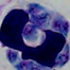

Photomicrograph. A white blood cell is seen. Captured at 1000x magnification.